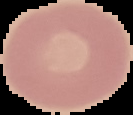

Summary:
  - Result: no malaria parasites detected
  - Image size: 133×115 pixels
  - Preparation: thin blood smear
  - Image type: segmented cell region on a black background